Report the malaria status of this cell.
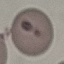

Uninfected.

Summary:
  - Capture: smartphone through the microscope eyepiece
  - Stain: Giemsa
  - Preparation: thin blood smear
  - Image type: cell patch, automatically extracted from a larger field of view and resized to 64 × 64 pixels